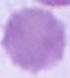

An erythrocyte is shown. Captured at 1000x magnification. Micrograph.